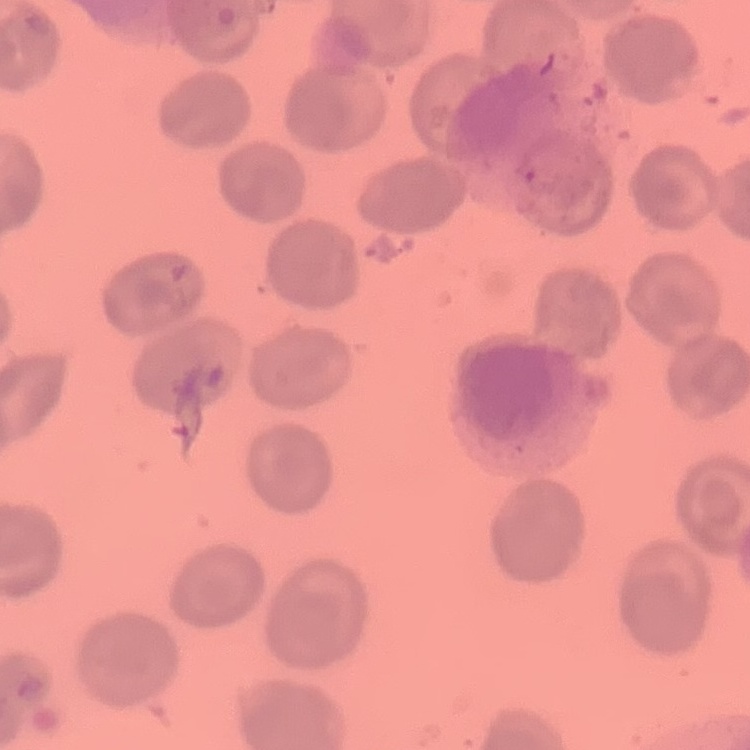

Summary:
  - Red blood cell morphology: no rouleaux formation
  - Image type: square crop of a larger photomicrograph
  - Preparation: thin peripheral smear
  - Stain: Field's or Giemsa